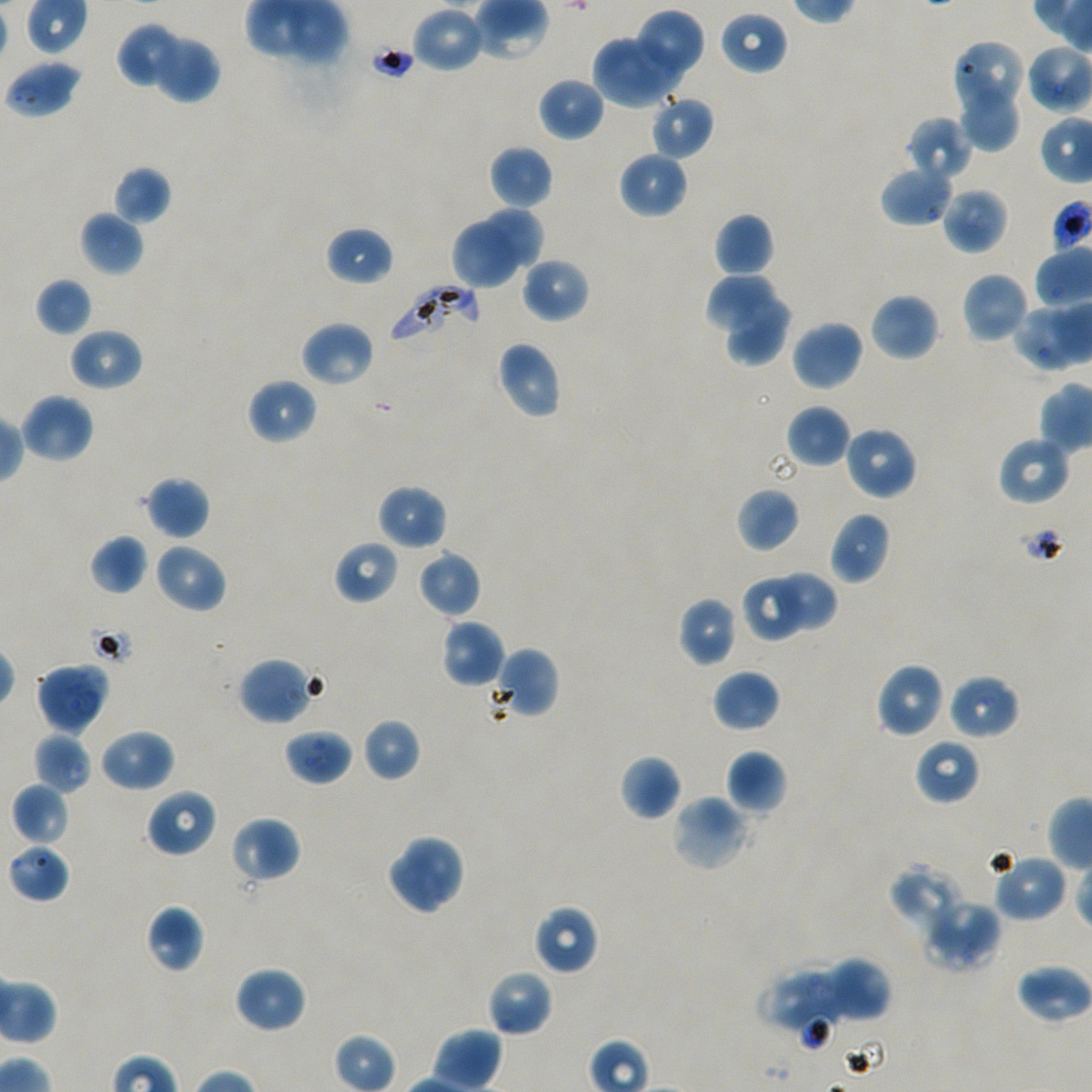

Not every red blood cell is marked.
field of view = single
preparation = thin blood smear
image size = 1092×1092 pixels
stain = Giemsa
objective = 100x, oil immersion, numerical aperture 1.45
locations of uninfected red blood cells = approximate bounding boxes as (x1, y1, x2, y2) in pixels: (411, 5, 486, 73), (640, 7, 704, 77), (719, 10, 789, 75), (117, 22, 183, 90), (148, 32, 221, 104), (592, 32, 682, 108), (952, 40, 1026, 119), (4, 58, 83, 120), (536, 77, 605, 142), (962, 88, 1019, 154), (651, 94, 714, 160), (906, 117, 972, 181), (489, 145, 553, 209), (617, 151, 689, 219), (880, 164, 954, 227), (112, 166, 171, 225), (941, 187, 1008, 255), (479, 206, 543, 268), (79, 210, 145, 277), (712, 212, 774, 278), (452, 221, 520, 289), (325, 226, 394, 286), (522, 257, 590, 323), (961, 272, 1030, 344), (706, 274, 777, 331), (35, 278, 93, 337), (727, 293, 793, 367), (869, 293, 940, 361), (1011, 303, 1084, 371), (790, 319, 864, 393), (299, 320, 376, 388), (68, 327, 143, 391), (494, 341, 562, 420), (247, 377, 317, 445), (18, 393, 95, 464), (786, 405, 851, 467), (843, 425, 919, 501), (996, 435, 1072, 507), (143, 476, 210, 540), (376, 484, 448, 551), (735, 487, 800, 553), (829, 511, 891, 585), (88, 533, 149, 596), (333, 540, 399, 604), (153, 543, 228, 614), (417, 550, 481, 619), (769, 571, 837, 634), (742, 573, 805, 644), (678, 596, 739, 666), (440, 619, 505, 688), (489, 647, 560, 720), (238, 656, 318, 726), (875, 662, 945, 738), (712, 669, 780, 733), (947, 674, 1020, 740), (361, 718, 421, 782), (98, 727, 175, 792), (33, 732, 92, 794), (915, 738, 981, 805), (725, 749, 787, 815), (619, 754, 681, 820), (11, 782, 70, 845), (145, 788, 218, 858), (670, 794, 750, 873), (230, 816, 300, 884), (385, 833, 467, 916), (8, 843, 70, 903), (991, 852, 1068, 923), (889, 862, 966, 929), (921, 898, 1002, 972), (145, 905, 204, 973), (533, 905, 599, 975), (820, 958, 891, 1023), (1015, 963, 1091, 1024), (234, 965, 307, 1034), (487, 969, 553, 1038), (775, 970, 843, 1031)
donor blood group = A+/O+
culture = P. falciparum strain NF54, static, in vitro
locations of red blood cells of indeterminate infection status = approximate bounding boxes as (x1, y1, x2, y2) in pixels: (35, 661, 111, 735), (284, 729, 353, 784)
locations of infected red blood cells = approximate bounding boxes as (x1, y1, x2, y2) in pixels: (387, 281, 481, 350)